Assess this cell for malaria.
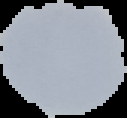
It is uninfected.

{
  "image_size": "127×118 pixels",
  "image_type": "cell region segmented out of the field of view; surrounding area masked to black",
  "preparation": "thin blood smear"
}